Locate every Plasmodium falciparum parasite and give its life-cycle stage, and locate every leukocyte and any debris.
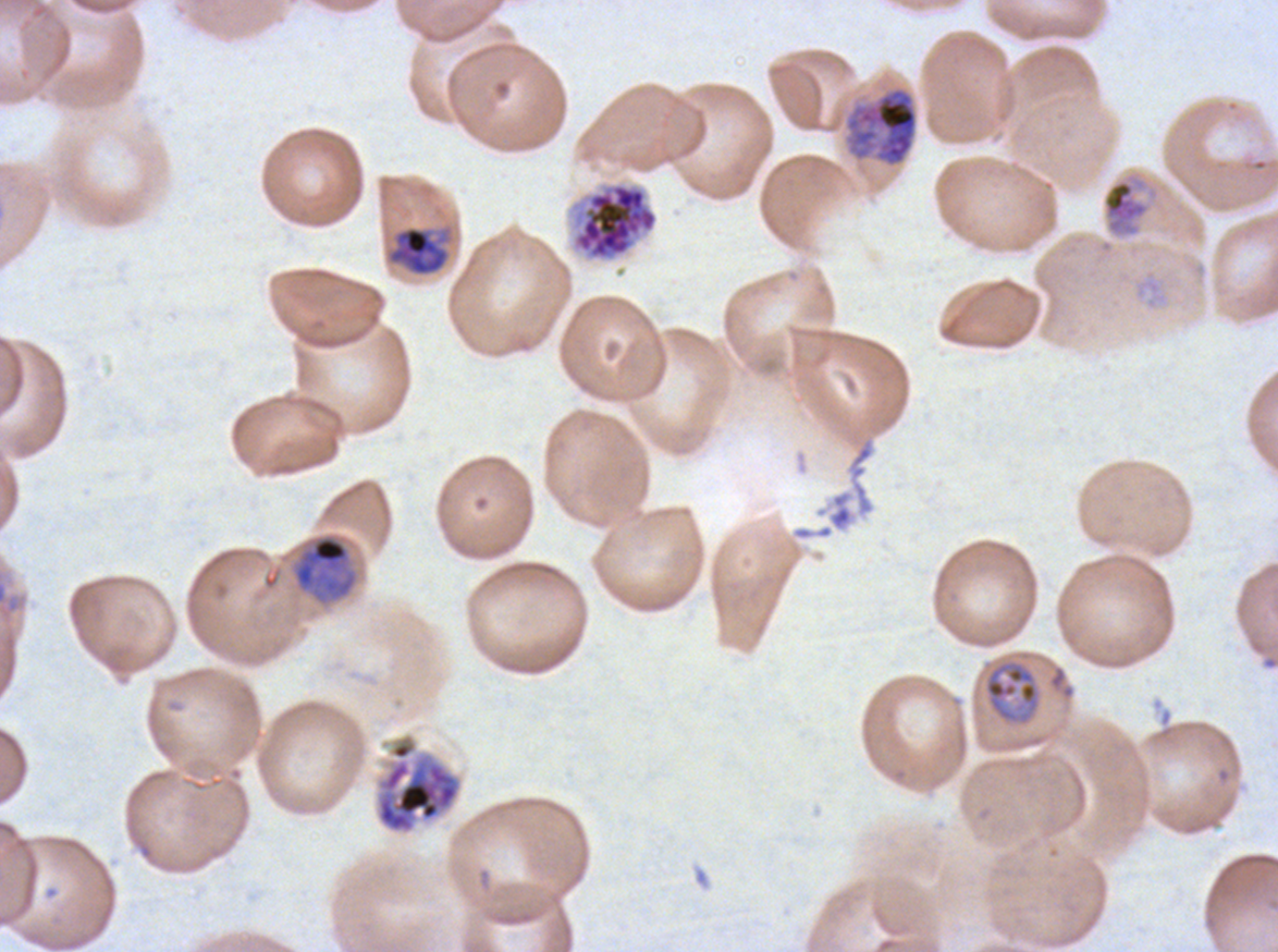
Approximate bounding boxes as {x1, y1, x2, y2} in pixels.
Mid trophozoites: {1100, 169, 1161, 239}, {983, 659, 1041, 725}.
Late trophozoites: {386, 225, 453, 277}, {291, 532, 359, 605}.
Early schizonts: {844, 86, 918, 167}, {375, 733, 462, 835}.
Segmenters: {571, 182, 658, 261}.
Debris: {791, 489, 854, 542}.
No rings, late-ring/early-trophozoite forms, late schizonts, gametocytes, or leukocytes observed.

field_of_view: sub-image separated from a larger composite
life_cycle_stages_observed: mid trophozoite, late trophozoite, early schizont, segmenter
stain: Giemsa
image_size: 1278×952 pixels
specimen: Plasmodium falciparum cultured ex vivo for 24 to 48 hours, from a patient in The Gambia
preparation: thin blood smear